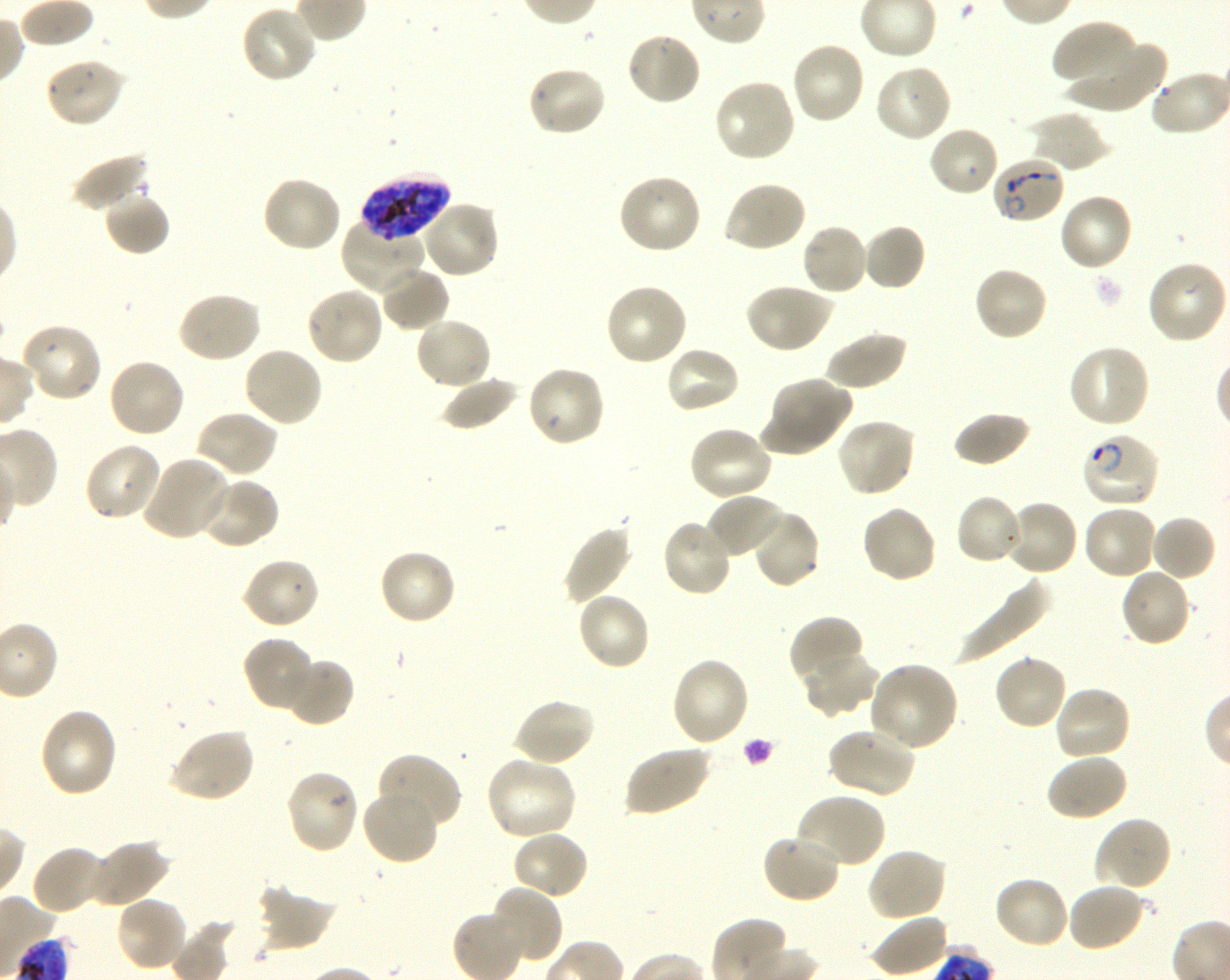

Approximate bounding boxes as [x1, y1, x2, y2] in pixels. Not every red blood cell is marked. A life-cycle stage — or a range of stages, where the recorded stages span more than one — follows each staged infected red blood cell.
Summary:
  - Locations of uninfected red blood cells: [240, 4, 318, 84], [1052, 19, 1138, 85], [625, 31, 702, 107], [1065, 36, 1167, 114], [790, 40, 866, 125], [43, 56, 126, 129], [873, 62, 953, 143], [525, 65, 607, 138], [713, 79, 798, 163], [1026, 110, 1111, 174], [927, 125, 1000, 198], [72, 152, 151, 214], [617, 172, 703, 256], [261, 174, 343, 254], [723, 180, 808, 255], [103, 190, 171, 256], [1057, 191, 1133, 272], [420, 200, 501, 279], [341, 219, 429, 296], [800, 222, 870, 296], [861, 224, 926, 293], [1146, 260, 1227, 345], [973, 265, 1049, 342], [378, 266, 451, 332], [604, 283, 689, 368], [745, 283, 833, 354], [305, 286, 385, 366], [177, 291, 262, 364], [414, 317, 494, 390], [20, 323, 103, 403], [824, 331, 907, 391], [1067, 344, 1152, 430], [242, 345, 324, 428], [663, 345, 742, 414], [107, 356, 186, 439], [524, 364, 607, 448], [441, 375, 520, 431], [763, 376, 851, 454], [194, 410, 278, 479], [953, 411, 1032, 468], [836, 417, 917, 498], [687, 426, 772, 503], [83, 442, 161, 523], [140, 456, 231, 541], [200, 476, 280, 550], [707, 494, 789, 562], [955, 494, 1025, 566], [1003, 498, 1080, 576], [860, 503, 937, 585], [1082, 505, 1158, 581], [750, 509, 821, 589], [1150, 515, 1217, 582], [661, 517, 734, 598], [561, 522, 633, 605], [377, 547, 457, 626], [240, 557, 320, 629], [1118, 566, 1192, 648], [956, 577, 1051, 664], [576, 591, 651, 672], [789, 616, 866, 687], [241, 635, 317, 712], [802, 649, 878, 716], [992, 652, 1069, 730], [281, 655, 355, 727], [670, 657, 750, 747], [869, 660, 959, 752], [1053, 684, 1133, 763], [511, 697, 595, 767], [38, 706, 119, 798], [168, 727, 255, 804], [826, 727, 916, 800], [623, 744, 712, 817], [1046, 753, 1129, 822], [376, 754, 462, 834], [484, 756, 578, 841], [285, 768, 360, 854], [362, 786, 440, 866], [796, 793, 886, 870], [1093, 816, 1173, 892], [512, 829, 590, 901], [760, 832, 842, 904], [88, 839, 169, 908], [30, 844, 108, 916], [865, 847, 947, 922], [993, 875, 1071, 950], [1066, 881, 1146, 953], [257, 882, 337, 953], [488, 885, 562, 965], [114, 896, 189, 973], [868, 913, 949, 977]
  - Locations of infected red blood cells: [991, 156, 1065, 225] ring; [361, 173, 450, 243] late trophozoite to late schizont; [1081, 432, 1162, 508] ring
  - Objective: 100x, oil immersion, numerical aperture 1.30
  - Donor blood group: O+
  - Preparation: thin blood smear
  - Culture: in-vitro P. falciparum strain 3D7, shaking
  - Image size: 1230×980 pixels
  - Field of view: single
  - Stain: Giemsa